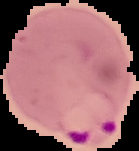
Image is 139×151 pixels. From a thin blood film. The area outside the segmented cell region is set to black. Result: malaria parasites detected.